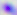

Summary:
  - Magnification: 400x
  - Modality: micrograph
  - Identification: Toxoplasma gondii